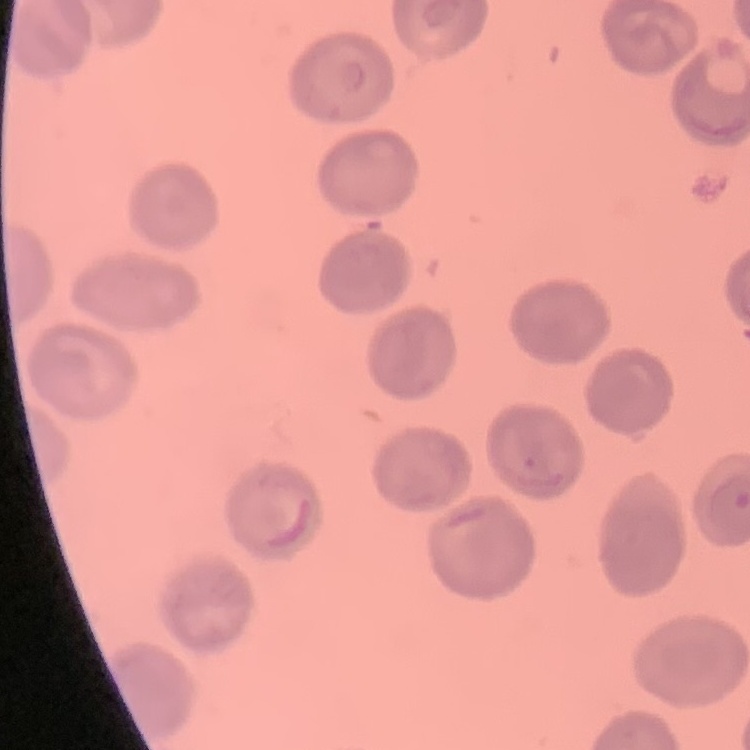

Summary:
  - Erythrocyte morphology: no rouleaux formation
  - Stain: Field's or Giemsa
  - Image type: square crop of a larger photomicrograph
  - Preparation: thin blood smear